Give the position of every malaria parasite, noting whether each is a trophozoite, schizont, or gametocyte.
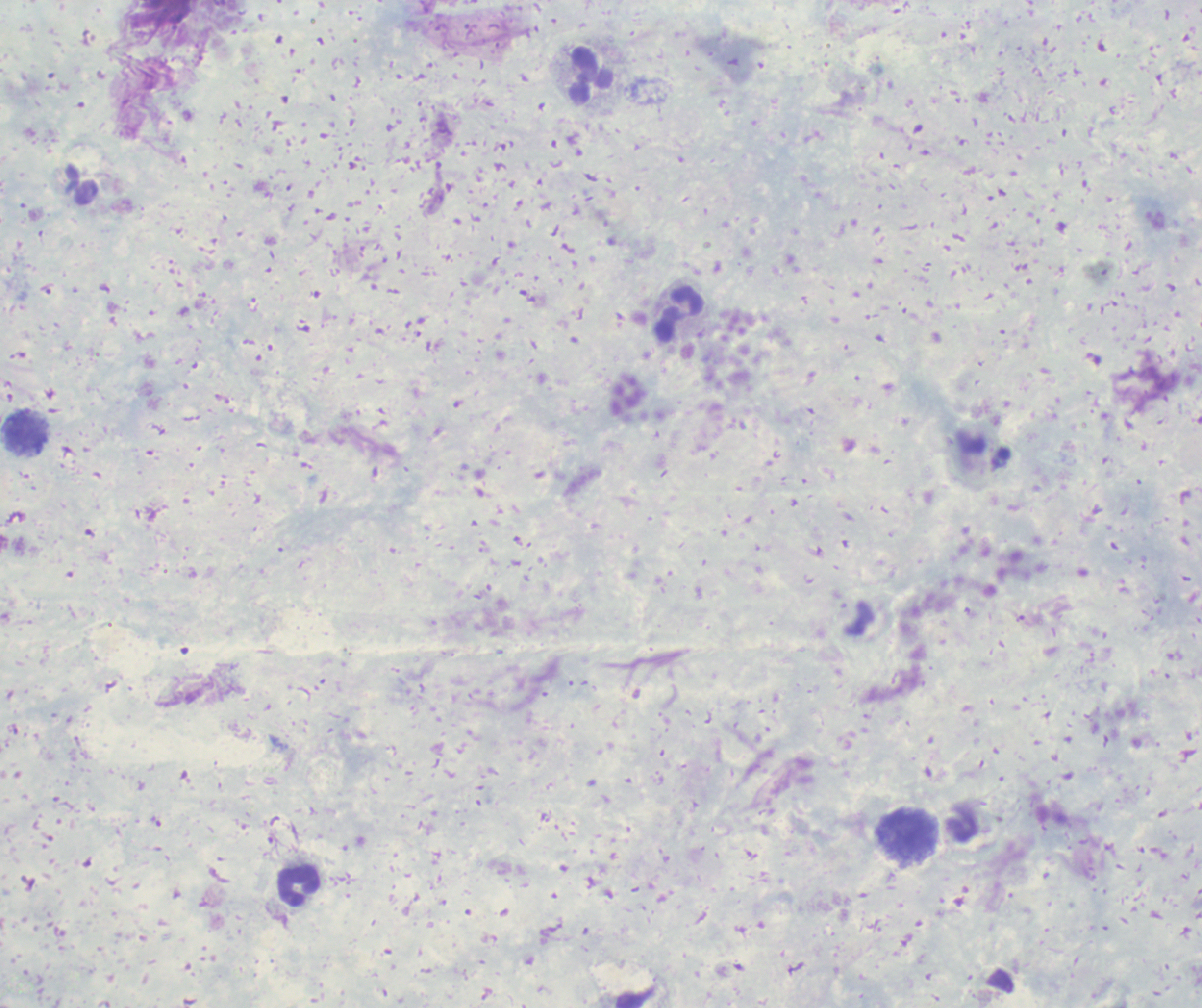
Negative for malaria parasites.

Approximate centers as (x, y) in pixels.
Summary:
  - Leukocyte locations: (592, 76), (679, 315), (25, 433), (908, 836), (299, 887)
  - Magnification: 100x
  - Context: previously used in a real diagnosis
  - Background quality: unsatisfactory
  - Stain: Romanowsky
  - Preparation: thick smear of blood
  - Image size: 1202×1008 pixels
  - Field of view: single